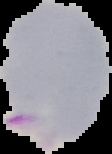

image type = segmented cell region with the area outside set to black
result = Plasmodium parasites detected
preparation = thin blood smear
image size = 112×154 pixels